Comment on the morphology of the erythrocytes.
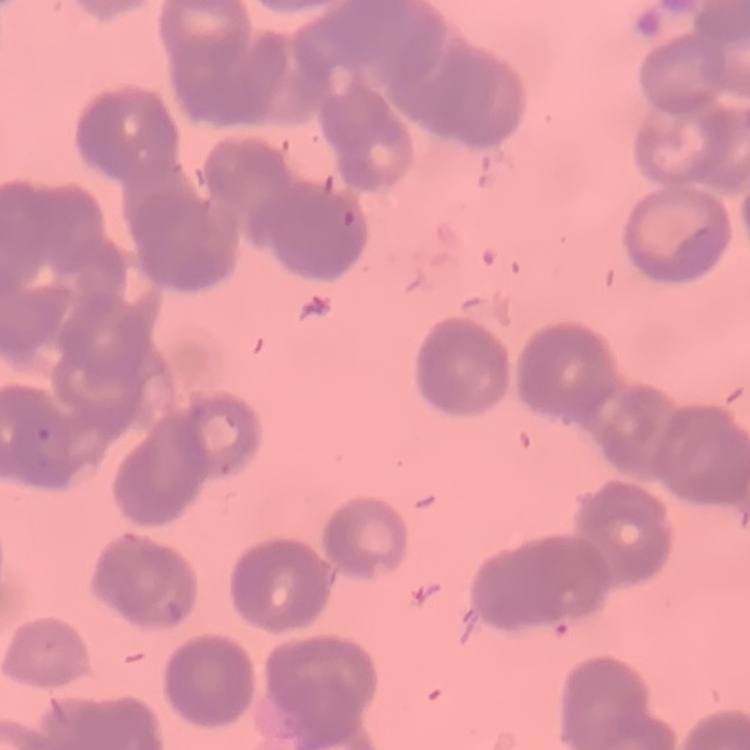

Rouleaux formation.

{
  "preparation": "thin blood smear",
  "image_type": "square crop of a larger photomicrograph",
  "stain": "Field's or Giemsa"
}